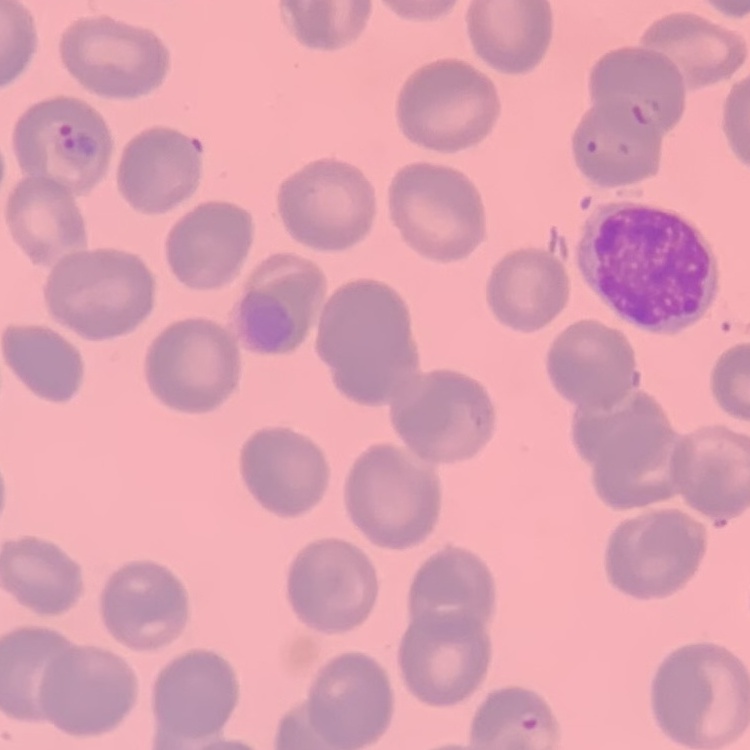

Summary:
  - Erythrocyte morphology: no rouleaux formation
  - Preparation: thin peripheral smear
  - Image type: square crop of a larger photomicrograph
  - Stain: Field's or Giemsa